Classify this cell by malaria status.
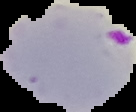
It is parasitized.

image type = segmented cell region on a black background
preparation = thin blood smear
image size = 136×112 pixels